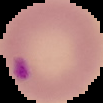
Summary:
  - Malaria status: parasitized
  - Image type: segmented cell region with the area outside set to black
  - Preparation: thin blood film
  - Image size: 103×103 pixels